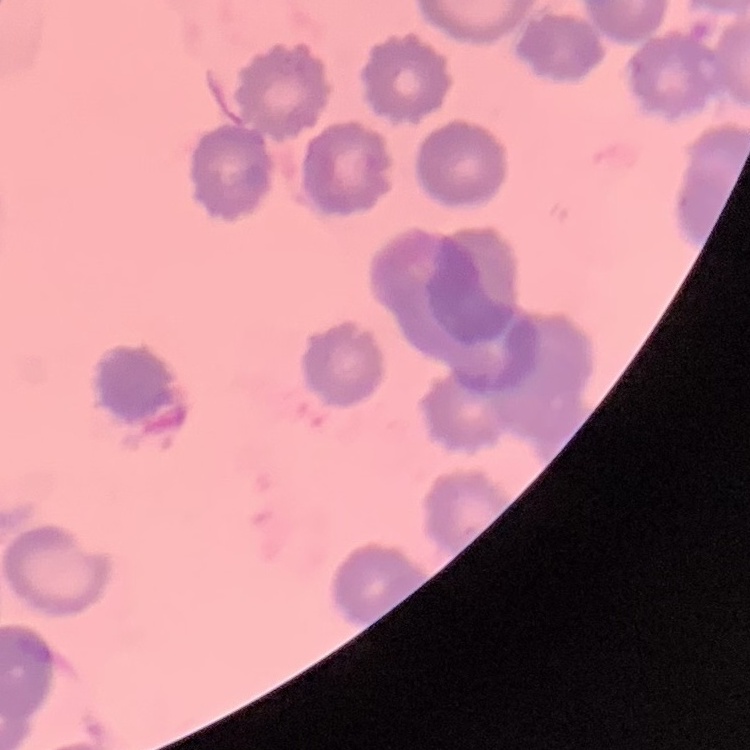
erythrocyte_morphology: no rouleaux formation
stain: Field's or Giemsa
preparation: thin peripheral smear
image_type: square crop of a larger photomicrograph